Report the malaria status of this cell.
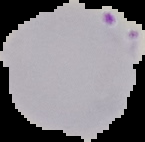
Parasitized.

image type = segmented cell region on a black background
preparation = thin blood smear
image size = 145×142 pixels